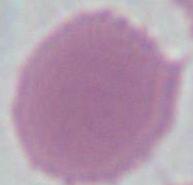

identification = erythrocyte
modality = micrograph
magnification = 1000x